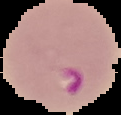
From a thin blood film. The area outside the segmented cell region is set to black. Malaria status: parasitized. Image is 121×115 pixels.